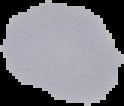

{
  "image_size": "124×106 pixels",
  "image_type": "cell region segmented out of the field of view; surrounding area masked to black",
  "malaria_status": "uninfected",
  "preparation": "thin blood smear"
}